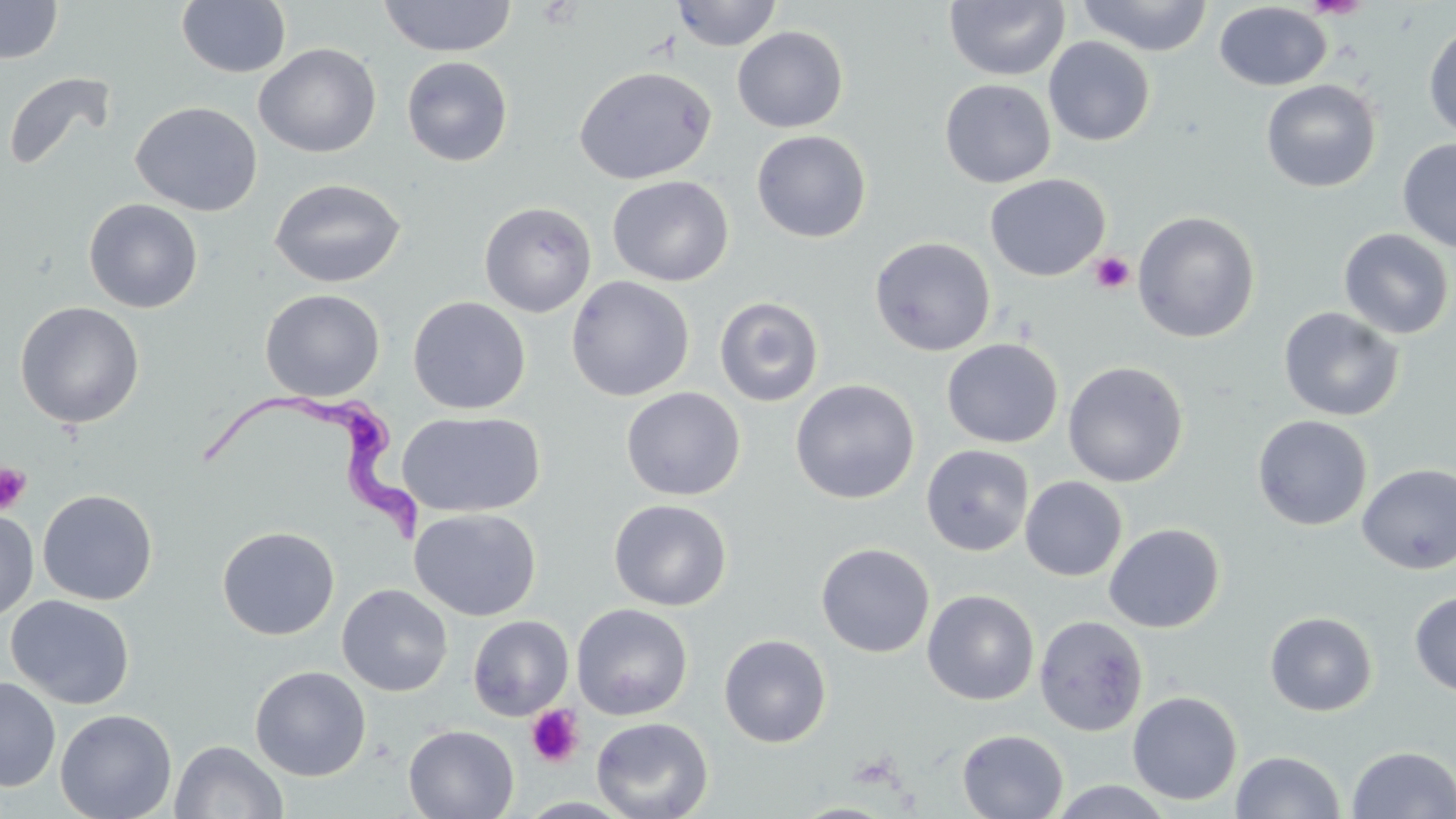

Summary:
  - Coordinate format: approximate bounding boxes as named x1/y1/x2/y2 corners in pixels
  - Trypanosoma brucei locations: (x1=198, y1=388, x2=428, y2=544)
  - Platelet locations: (x1=1090, y1=251, x2=1134, y2=295), (x1=0, y1=462, x2=32, y2=514), (x1=526, y1=704, x2=584, y2=768)
  - Uninfected red blood cell locations: (x1=378, y1=0, x2=517, y2=58), (x1=671, y1=0, x2=784, y2=52), (x1=1076, y1=0, x2=1214, y2=57), (x1=0, y1=1, x2=62, y2=64), (x1=176, y1=1, x2=292, y2=78), (x1=943, y1=1, x2=1071, y2=82), (x1=1214, y1=2, x2=1332, y2=91), (x1=1423, y1=22, x2=1456, y2=140), (x1=732, y1=26, x2=848, y2=133), (x1=1043, y1=37, x2=1155, y2=146), (x1=254, y1=43, x2=381, y2=158), (x1=402, y1=56, x2=513, y2=167), (x1=573, y1=65, x2=716, y2=184), (x1=3, y1=72, x2=116, y2=173), (x1=940, y1=78, x2=1057, y2=188), (x1=1260, y1=79, x2=1382, y2=193), (x1=131, y1=101, x2=263, y2=217), (x1=751, y1=130, x2=872, y2=243), (x1=1397, y1=138, x2=1456, y2=252), (x1=984, y1=173, x2=1110, y2=281), (x1=607, y1=175, x2=734, y2=286), (x1=269, y1=178, x2=406, y2=288), (x1=83, y1=198, x2=203, y2=313), (x1=479, y1=201, x2=596, y2=317), (x1=1132, y1=210, x2=1261, y2=343), (x1=1338, y1=228, x2=1455, y2=340), (x1=869, y1=236, x2=996, y2=356), (x1=566, y1=275, x2=695, y2=402), (x1=260, y1=288, x2=385, y2=401), (x1=408, y1=296, x2=531, y2=414), (x1=714, y1=296, x2=824, y2=408), (x1=14, y1=301, x2=145, y2=429), (x1=1278, y1=307, x2=1405, y2=422), (x1=942, y1=338, x2=1063, y2=448), (x1=1063, y1=361, x2=1189, y2=488), (x1=790, y1=379, x2=920, y2=504), (x1=621, y1=387, x2=745, y2=501), (x1=396, y1=411, x2=546, y2=518), (x1=1252, y1=414, x2=1373, y2=531), (x1=921, y1=444, x2=1034, y2=557), (x1=1357, y1=464, x2=1456, y2=575), (x1=1020, y1=476, x2=1127, y2=581), (x1=37, y1=489, x2=158, y2=605), (x1=609, y1=499, x2=732, y2=611), (x1=409, y1=507, x2=541, y2=621), (x1=0, y1=508, x2=40, y2=621), (x1=1103, y1=523, x2=1225, y2=633), (x1=216, y1=525, x2=340, y2=640), (x1=816, y1=542, x2=935, y2=658), (x1=336, y1=584, x2=453, y2=697), (x1=922, y1=589, x2=1040, y2=705), (x1=1409, y1=591, x2=1456, y2=697), (x1=6, y1=594, x2=135, y2=709), (x1=571, y1=603, x2=693, y2=721), (x1=1264, y1=611, x2=1377, y2=716), (x1=468, y1=615, x2=574, y2=720), (x1=1034, y1=615, x2=1148, y2=736), (x1=718, y1=634, x2=832, y2=747), (x1=249, y1=665, x2=371, y2=781), (x1=0, y1=677, x2=61, y2=791), (x1=1127, y1=690, x2=1243, y2=806), (x1=54, y1=708, x2=177, y2=819), (x1=591, y1=716, x2=713, y2=819), (x1=403, y1=724, x2=519, y2=818), (x1=956, y1=729, x2=1069, y2=818), (x1=170, y1=740, x2=288, y2=819), (x1=1346, y1=746, x2=1456, y2=818), (x1=1231, y1=750, x2=1345, y2=819), (x1=1048, y1=780, x2=1176, y2=818), (x1=791, y1=802, x2=897, y2=819)
  - Slide-level diagnosis: Trypanosoma brucei
  - Field of view: single
  - Modality: optical microscopy
  - Preparation: thin blood film
  - Image size: 1456×819 pixels
  - Magnification: 1000x
  - Stain: May-Grünwald-Giemsa